Classify this cell by malaria status.
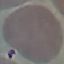

Uninfected.

Thin blood film. Photographed with a smartphone camera at the microscope eyepiece. Automatically extracted cell patch, resized to 64 × 64 pixels. Giemsa-stained preparation.